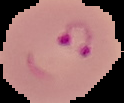

Summary:
  - Result: malaria parasites identified
  - Image size: 124×103 pixels
  - Image type: segmented cell region with the area outside set to black
  - Preparation: thin blood film